Name the cell type shown.
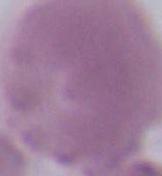

An erythrocyte.

modality = micrograph
magnification = 1000x